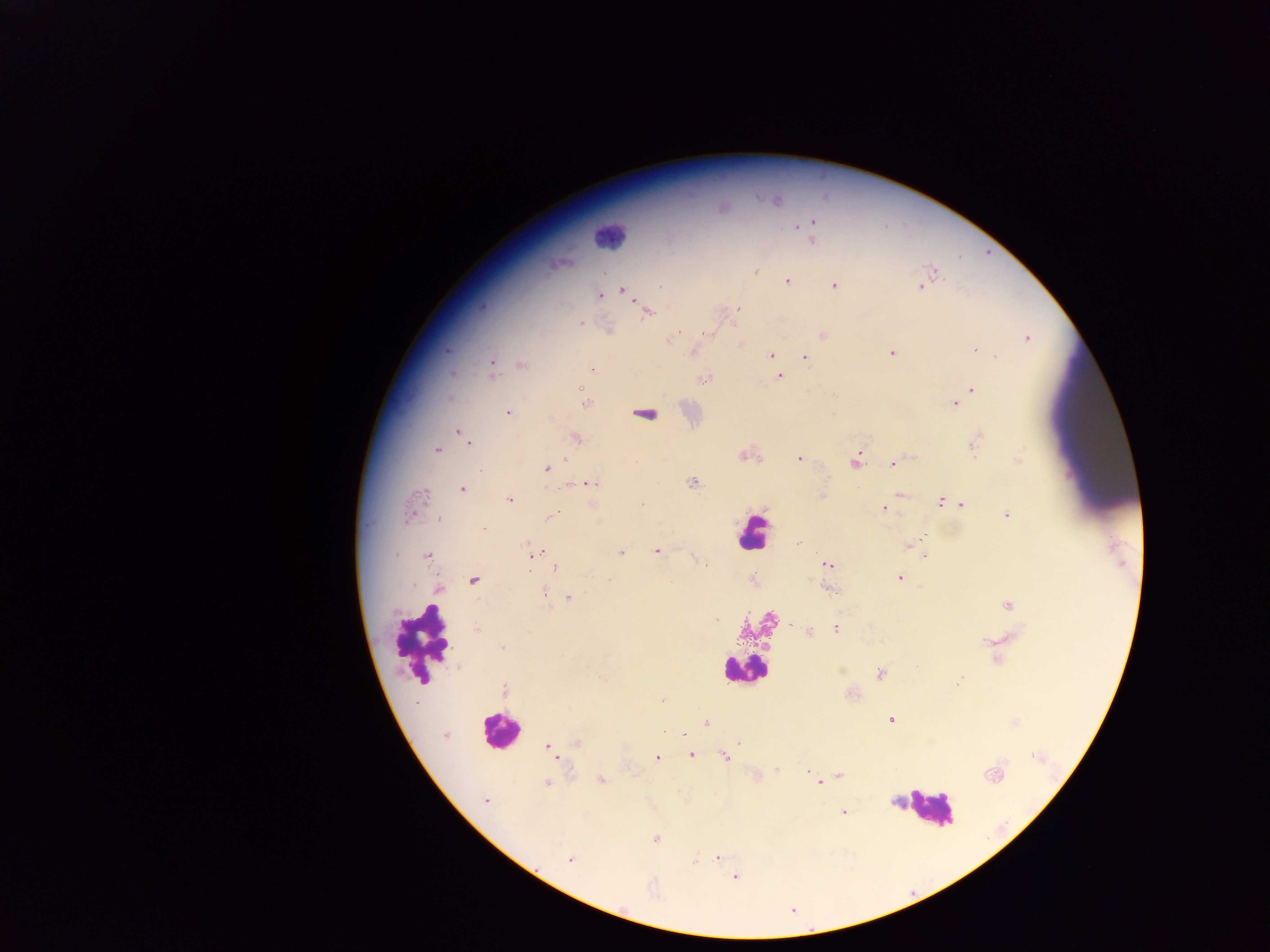

preparation: thick blood smear
field_of_view: single
image_size: 1270×952 pixels
capture: mobile-phone photograph through a microscope
leukocyte_locations: 'approximate centers as (x, y) in pixels: (606, 236), (752, 534), (424, 641), (742, 670), (499, 730), (930, 807)'
malaria_parasite_locations: 'approximate centers as (x, y) in pixels: (777, 201), (813, 223), (811, 240), (558, 263), (756, 270), (934, 271), (787, 281), (835, 286), (921, 286), (623, 290), (599, 295), (482, 307), (738, 309), (647, 313), (579, 324), (705, 333), (823, 335), (673, 338), (1027, 339), (976, 349), (693, 350), (891, 352), (770, 355), (996, 357), (805, 358), (492, 364), (522, 365), (591, 369), (492, 372), (451, 373), (780, 376), (704, 380), (971, 389), (584, 396), (448, 398), (586, 403), (954, 404), (508, 413), (647, 415), (550, 420), (460, 432), (575, 438), (469, 442), (974, 444), (437, 449), (742, 455), (799, 458), (1018, 461), (855, 463), (893, 464), (546, 468), (692, 482), (590, 483), (462, 490), (902, 494), (822, 497), (509, 500), (418, 501), (940, 502), (962, 504), (884, 508), (412, 510), (1006, 515), (551, 516), (439, 520), (483, 529), (798, 543), (911, 544), (657, 550), (534, 553), (620, 553), (427, 556), (925, 556), (827, 563), (555, 568), (898, 578), (474, 580), (610, 580), (440, 589), (830, 589), (544, 592), (569, 597), (1008, 605), (716, 619), (835, 628), (809, 631), (502, 647), (879, 674), (960, 680), (504, 691), (662, 700), (891, 719), (706, 722), (445, 735), (684, 735), (739, 742), (576, 744), (548, 746), (553, 755), (691, 755), (725, 756), (657, 758), (777, 769), (808, 772), (993, 775), (757, 776), (839, 776), (601, 779), (546, 783), (819, 783), (485, 799), (843, 812), (655, 839), (717, 857), (570, 860), (694, 861), (735, 877)'
country: Ghana